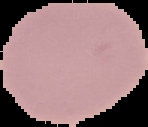

preparation = thin blood smear
image type = cell region segmented out of the field of view; surrounding area masked to black
image size = 148×127 pixels
malaria status = uninfected